Describe the morphology of the red blood cells.
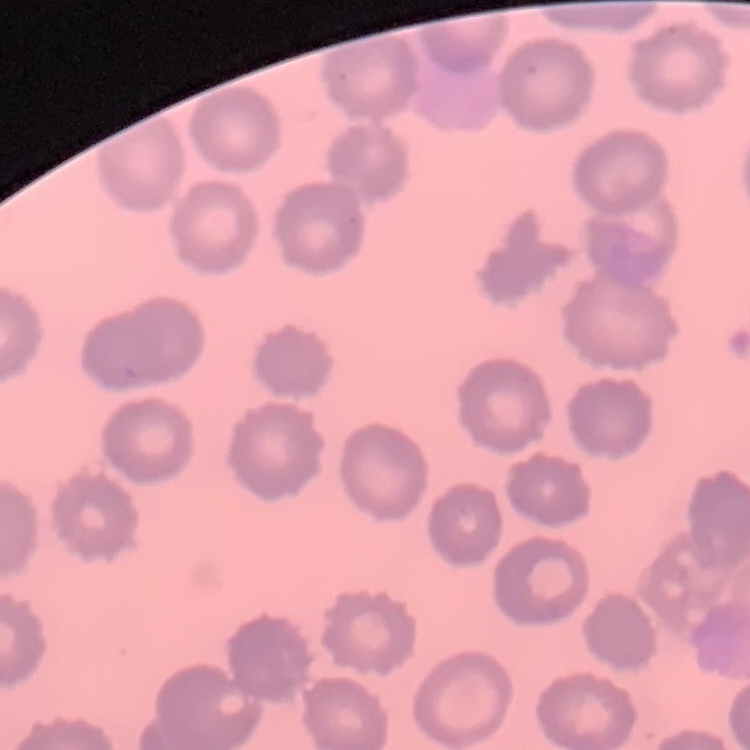
No rouleaux formation.

One tile cut from a larger photomicrograph. Thin peripheral smear. Field's or Giemsa stain.